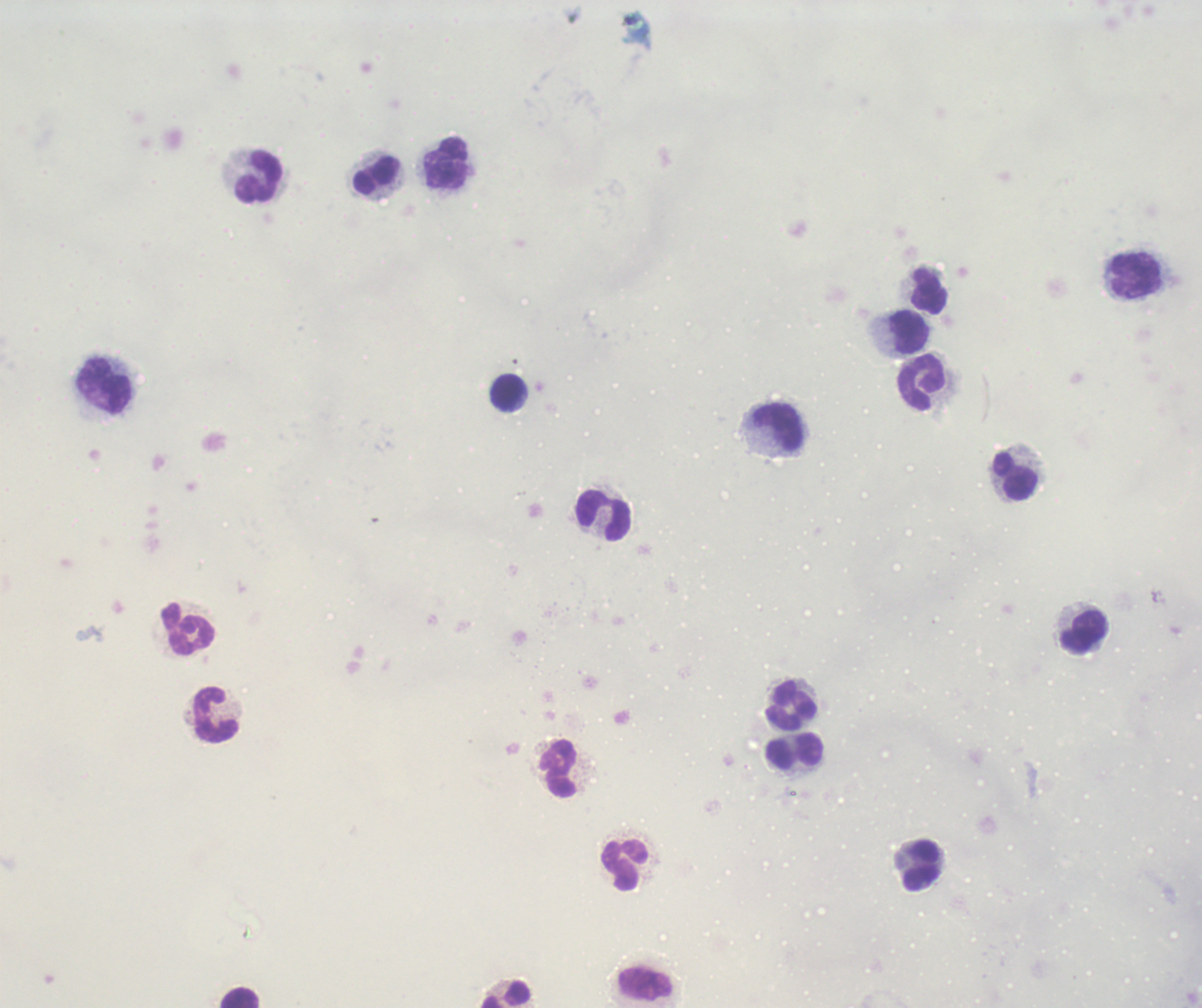 Approximate centers as {x, y} in pixels. Leukocyte locations: {446, 164}, {378, 176}, {259, 178}, {1136, 276}, {929, 293}, {909, 333}, {921, 383}, {104, 386}, {508, 393}, {777, 427}, {1015, 477}, {603, 516}, {189, 629}, {1084, 633}, {791, 706}, {216, 715}, {796, 750}, {558, 769}, {625, 865}, {920, 865}, {647, 985}, {506, 995}, {241, 998}. Result: negative for malaria parasites. Romanowsky stain. Thick blood film. Background quality: poor. 100x magnification. One field from this slide. Image is 1202×1008 pixels. Previously used in a real diagnosis.